Classify this cell by malaria status.
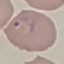

It is parasitized.

stain = Giemsa
image type = cell patch, automatically extracted from a larger field of view and resized to 64 × 64 pixels
capture = smartphone through the microscope eyepiece
preparation = thin smear